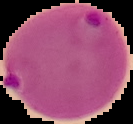

Summary:
  - Preparation: thin blood film
  - Malaria status: parasitized
  - Image size: 133×124 pixels
  - Image type: segmented cell region on a black background